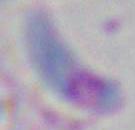
{
  "identification": "Toxoplasma gondii",
  "modality": "photomicrograph",
  "magnification": "1000x"
}